Name the cell type shown.
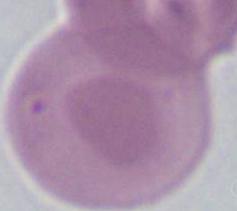
An erythrocyte.

Photomicrograph. Captured at 1000x magnification.